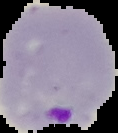

image type = segmented cell region on a black background
malaria status = parasitized
image size = 118×133 pixels
preparation = thin blood smear